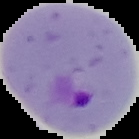
{
  "image_type": "cell region segmented out of the field of view; surrounding area masked to black",
  "image_size": "139×139 pixels",
  "malaria_status": "parasitized",
  "preparation": "thin blood film"
}